Draw a bounding box around every malaria parasite, every leukocyte, and every artifact (stain precipitate or debris).
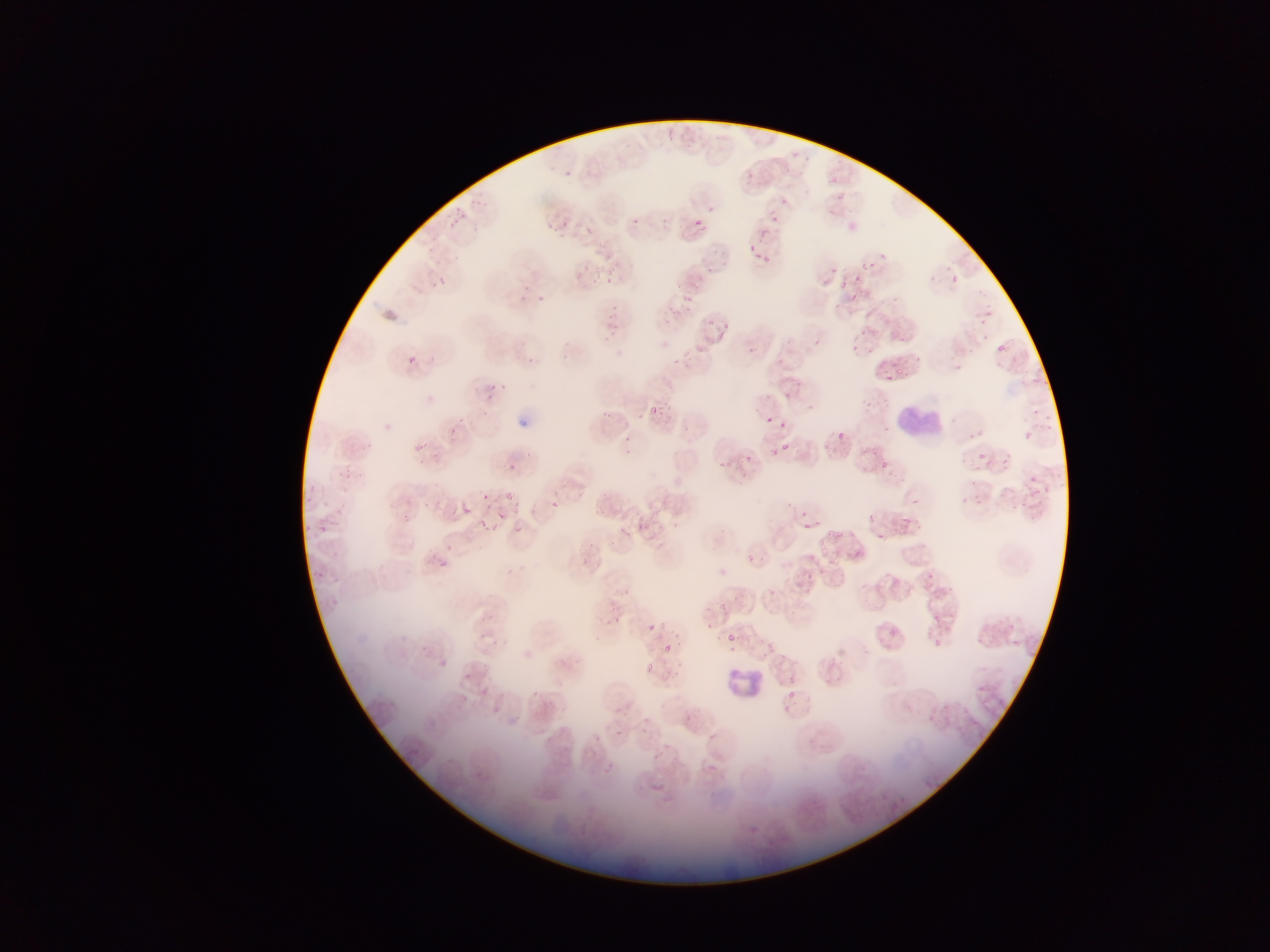
Approximate bounding boxes as {left, top, right, bottom} in pixels.
Malaria parasites: {563, 170, 571, 177}, {743, 171, 760, 185}, {831, 175, 841, 187}, {839, 195, 847, 201}, {779, 196, 792, 204}, {709, 204, 717, 212}, {452, 210, 466, 227}, {769, 212, 780, 223}, {556, 214, 566, 225}, {665, 215, 674, 226}, {631, 217, 642, 228}, {691, 217, 707, 233}, {549, 222, 559, 233}, {584, 226, 595, 236}, {747, 244, 760, 249}, {764, 256, 772, 266}, {581, 263, 590, 275}, {605, 267, 618, 276}, {851, 272, 862, 283}, {950, 273, 960, 284}, {606, 275, 616, 288}, {435, 276, 449, 288}, {843, 280, 850, 288}, {535, 294, 544, 302}, {684, 294, 692, 302}, {606, 309, 614, 322}, {705, 311, 712, 328}, {978, 318, 989, 326}, {723, 319, 730, 330}, {860, 328, 868, 337}, {715, 331, 725, 342}, {852, 340, 863, 353}, {695, 344, 703, 353}, {1001, 345, 1009, 355}, {748, 346, 759, 356}, {406, 353, 418, 364}, {914, 353, 925, 360}, {898, 364, 909, 377}, {956, 365, 966, 376}, {885, 372, 891, 380}, {490, 384, 501, 391}, {784, 389, 795, 400}, {765, 390, 775, 398}, {485, 392, 493, 404}, {651, 404, 663, 416}, {1032, 408, 1041, 416}, {601, 409, 612, 422}, {480, 410, 487, 421}, {637, 412, 643, 421}, {460, 417, 467, 425}, {779, 421, 787, 429}, {446, 429, 455, 439}, {839, 429, 845, 442}, {1019, 430, 1033, 437}, {626, 438, 634, 443}, {415, 442, 430, 454}, {782, 442, 791, 451}, {771, 445, 781, 459}, {625, 448, 636, 453}, {977, 451, 985, 459}, {746, 454, 759, 468}, {997, 455, 1006, 465}, {718, 460, 729, 470}, {879, 461, 888, 469}, {508, 464, 516, 475}, {343, 468, 357, 482}, {1030, 476, 1037, 484}, {1046, 485, 1053, 495}, {310, 486, 320, 494}, {483, 492, 490, 500}, {506, 493, 516, 501}, {975, 494, 988, 505}, {912, 496, 919, 504}, {960, 496, 974, 507}, {551, 498, 558, 508}, {305, 499, 312, 508}, {422, 502, 431, 510}, {512, 503, 525, 514}, {462, 504, 473, 514}, {490, 504, 498, 511}, {654, 504, 675, 514}, {595, 505, 612, 516}, {863, 508, 871, 518}, {802, 509, 810, 516}, {641, 512, 655, 522}, {497, 513, 505, 523}, {405, 515, 413, 523}, {901, 515, 911, 524}, {480, 518, 490, 529}, {626, 521, 638, 534}, {513, 523, 523, 533}, {805, 523, 815, 531}, {320, 524, 328, 531}, {831, 528, 844, 542}, {877, 531, 885, 541}, {816, 540, 829, 549}, {444, 543, 454, 552}, {855, 546, 866, 556}, {746, 552, 753, 560}, {802, 553, 818, 561}, {830, 558, 837, 566}, {438, 562, 446, 567}, {801, 570, 815, 579}, {804, 586, 814, 597}, {766, 590, 778, 596}, {719, 599, 730, 609}, {933, 613, 940, 621}, {940, 620, 952, 631}, {646, 621, 657, 631}, {1007, 621, 1018, 631}, {926, 627, 937, 636}, {725, 632, 741, 641}, {931, 637, 946, 647}, {768, 639, 779, 658}, {661, 643, 678, 653}, {439, 658, 450, 668}, {645, 661, 655, 677}, {783, 675, 799, 682}, {787, 691, 798, 698}, {616, 728, 624, 736}, {664, 742, 673, 751}, {651, 751, 660, 761} | approximate {x, y} pixel centers of objects too small to bound: {588, 170}, {867, 263}, {769, 418}, {329, 505}, {931, 575}.
Leukocytes: {898, 392, 947, 439}, {725, 653, 765, 704}.

Summary:
  - Field of view: single
  - Image size: 1270×952 pixels
  - Country: Ghana
  - Preparation: thin blood film
  - Capture: mobile-phone photograph through a microscope